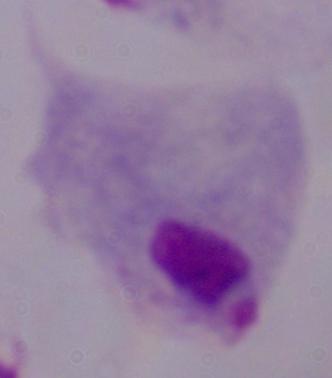

Summary:
  - Magnification: 1000x
  - Modality: micrograph
  - Identification: trichomonad